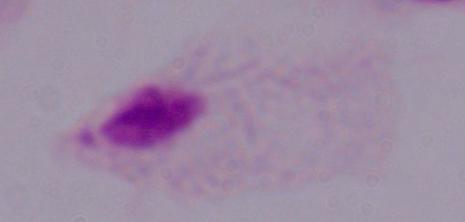
Summary:
  - Modality: photomicrograph
  - Magnification: 1000x
  - Identification: trichomonad